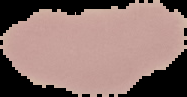

preparation: thin blood film
image_type: cell region segmented out of the field of view; surrounding area masked to black
result: negative for Plasmodium parasites
image_size: 187×97 pixels